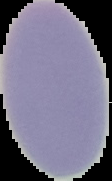
From a thin blood film. Malaria status: uninfected. Image is 112×181 pixels. The area outside the segmented cell region is set to black.